Locate every blood parasite and identify its species.
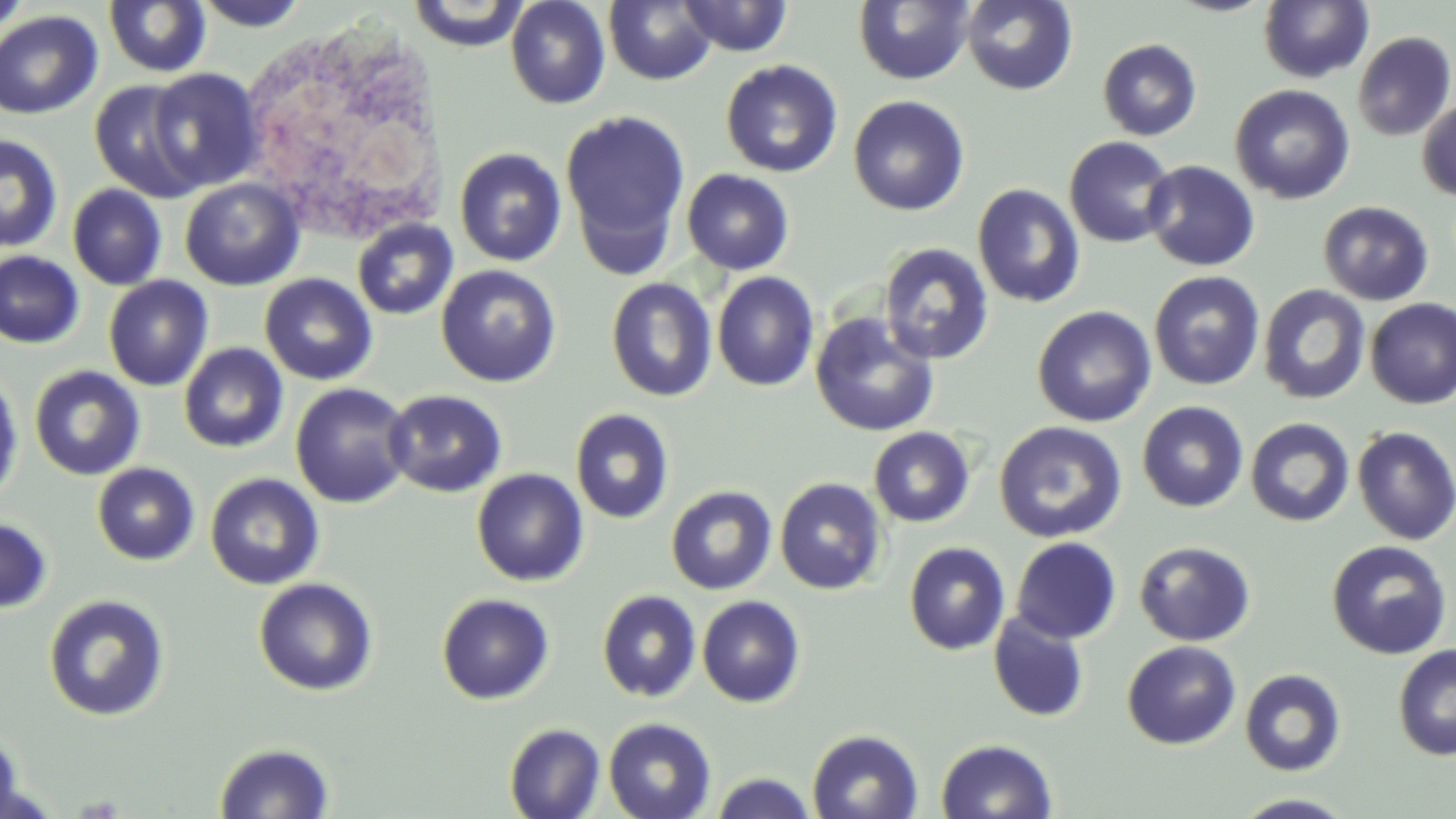

No blood parasites observed.

Approximate bounding boxes as [x1, y1, x2, y2] in pixels. White blood cell locations: [237, 14, 450, 251]. Uninfected red blood cell locations: [190, 0, 313, 31], [505, 0, 610, 109], [676, 0, 794, 57], [961, 0, 1078, 95], [1258, 0, 1375, 84], [1, 1, 34, 36], [103, 1, 211, 78], [406, 1, 533, 50], [603, 1, 717, 86], [853, 1, 976, 85], [0, 10, 103, 119], [1352, 30, 1456, 141], [1097, 38, 1202, 141], [720, 60, 843, 178], [146, 68, 264, 193], [88, 80, 207, 203], [1230, 84, 1355, 205], [848, 95, 970, 216], [1417, 98, 1456, 201], [559, 110, 691, 266], [0, 134, 64, 253], [1063, 136, 1178, 248], [454, 147, 567, 267], [1141, 160, 1260, 271], [681, 168, 794, 275], [179, 178, 305, 291], [972, 183, 1085, 308], [67, 184, 167, 290], [1318, 201, 1434, 305], [352, 218, 458, 320], [877, 241, 995, 365], [0, 250, 85, 349], [436, 264, 561, 387], [712, 271, 820, 391], [1148, 271, 1265, 391], [259, 273, 378, 385], [103, 275, 214, 391], [606, 278, 717, 402], [1257, 283, 1372, 404], [1365, 298, 1456, 408], [1032, 305, 1157, 427], [809, 311, 940, 437], [179, 343, 288, 453], [29, 365, 145, 481], [0, 370, 24, 506], [290, 382, 414, 508], [383, 389, 507, 498], [1137, 400, 1249, 512], [570, 408, 674, 524], [1245, 417, 1355, 527], [994, 421, 1127, 543], [868, 426, 975, 528], [1352, 426, 1456, 545], [92, 463, 200, 566], [471, 468, 589, 587], [204, 472, 325, 591], [775, 477, 887, 595], [665, 485, 777, 595], [0, 516, 54, 615], [1010, 537, 1122, 644], [1134, 540, 1256, 646], [1326, 540, 1453, 658], [903, 541, 1011, 655], [253, 578, 378, 696], [597, 590, 702, 702], [436, 593, 555, 705], [43, 594, 170, 721], [696, 595, 805, 708], [988, 611, 1089, 722], [1122, 641, 1241, 750], [1393, 644, 1456, 761], [1239, 669, 1346, 776], [602, 717, 717, 819], [503, 722, 605, 819], [806, 729, 924, 818], [0, 731, 32, 819], [935, 737, 1057, 819], [213, 741, 335, 819], [708, 771, 819, 819], [1229, 793, 1360, 818]. Slide-level diagnosis: no evidence of blood parasites. Thin blood smear. Image is 1456×819 pixels. One field of a larger specimen. Captured at 1000x magnification. Light microscopy. May-Grünwald-Giemsa-stained preparation.